Report the malaria status of this cell.
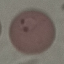
It is parasitized.

Summary:
  - Stain: Giemsa
  - Capture: smartphone camera at the microscope eyepiece
  - Preparation: thin blood film
  - Image type: automatically extracted cell patch, resized to 64 × 64 pixels